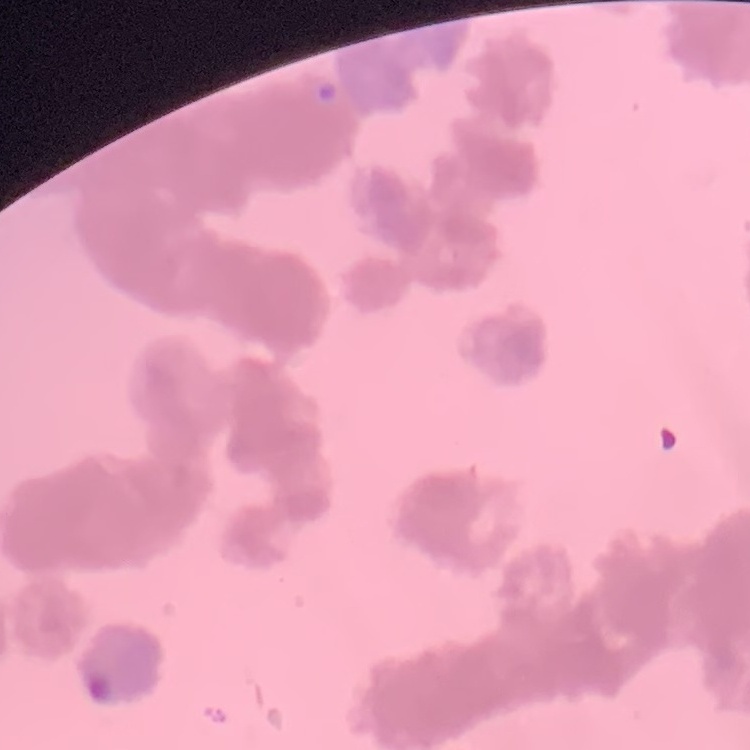
The red blood cells exhibit rouleaux formation. Field's or Giemsa stain. Square crop of a larger photomicrograph. Thin peripheral smear.